Comment on the morphology of the red blood cells.
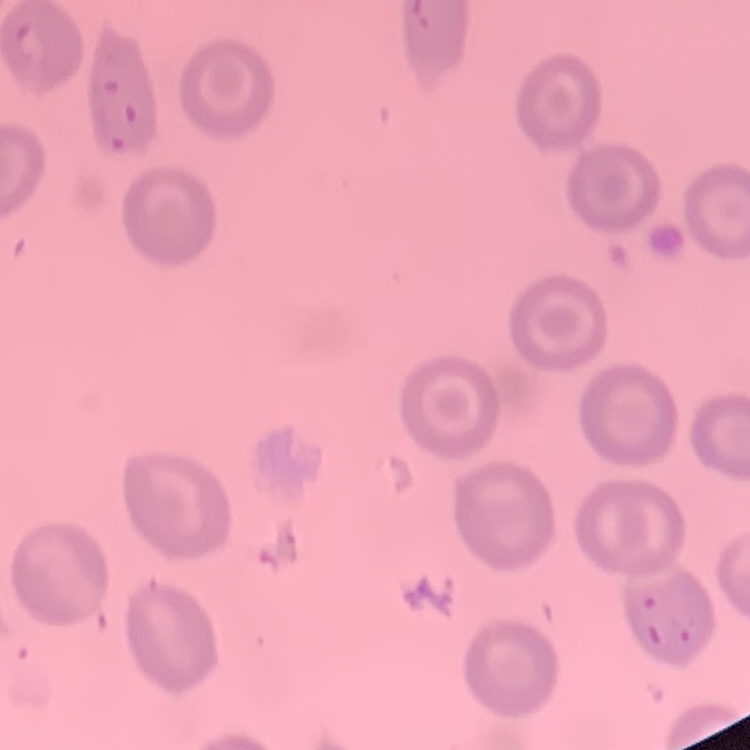

They show no rouleaux formation.

stain = Field's or Giemsa
image type = one tile cut from a larger photomicrograph
preparation = thin peripheral smear